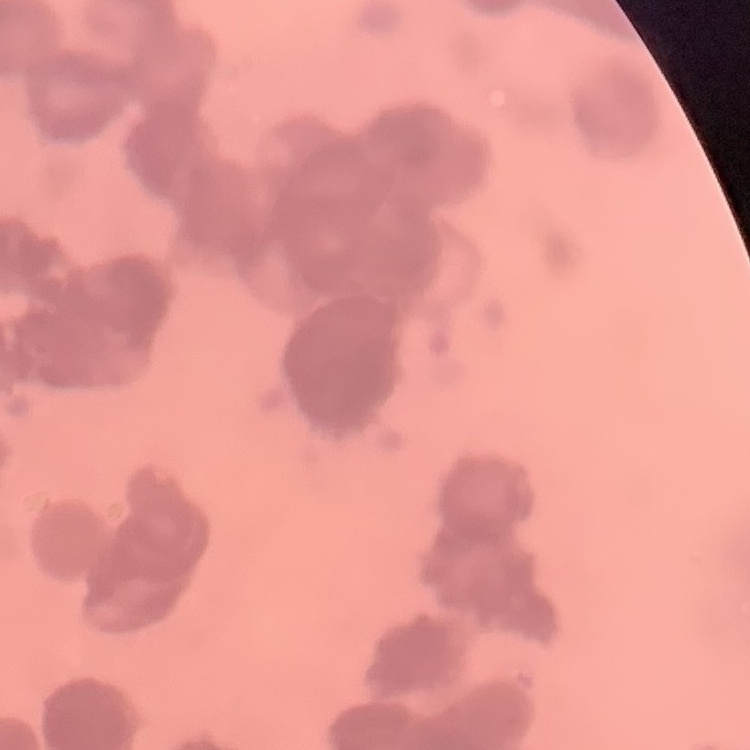
red blood cell morphology = rouleaux formation
stain = Field's or Giemsa
preparation = thin blood smear
image type = square crop of a larger photomicrograph